Report the malaria status of this cell.
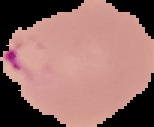
Parasitized.

Image is 154×127 pixels. Cell region segmented out of the field of view; the surrounding area is masked to black. From a thin blood smear.